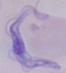
A trypanosome is seen. Captured at 1000x magnification. Photomicrograph.